Assess the morphology of the erythrocytes.
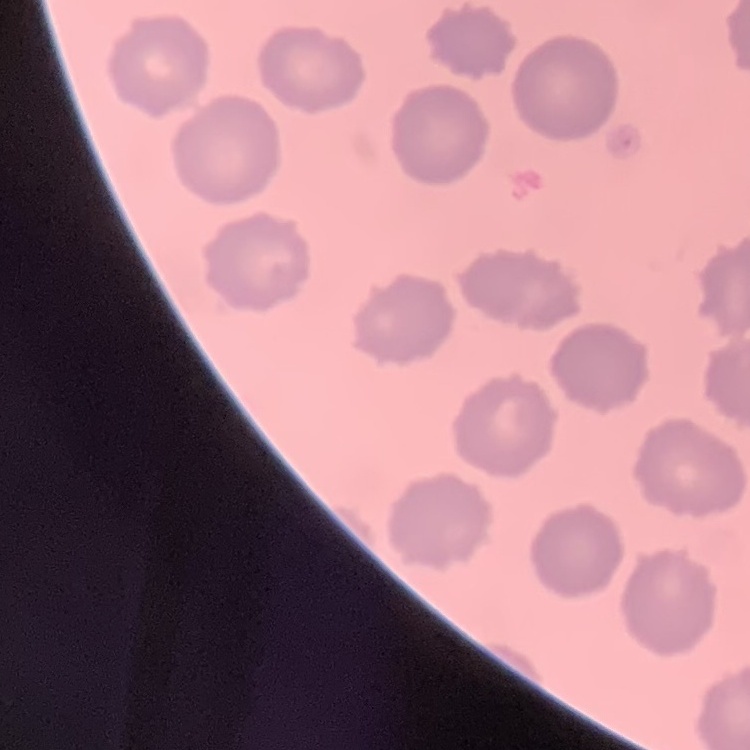
No rouleaux formation.

image type = square crop of a larger photomicrograph
preparation = thin peripheral smear
stain = Field's or Giemsa